Give the extent of all Plasmodium vivax-infected red blood cells.
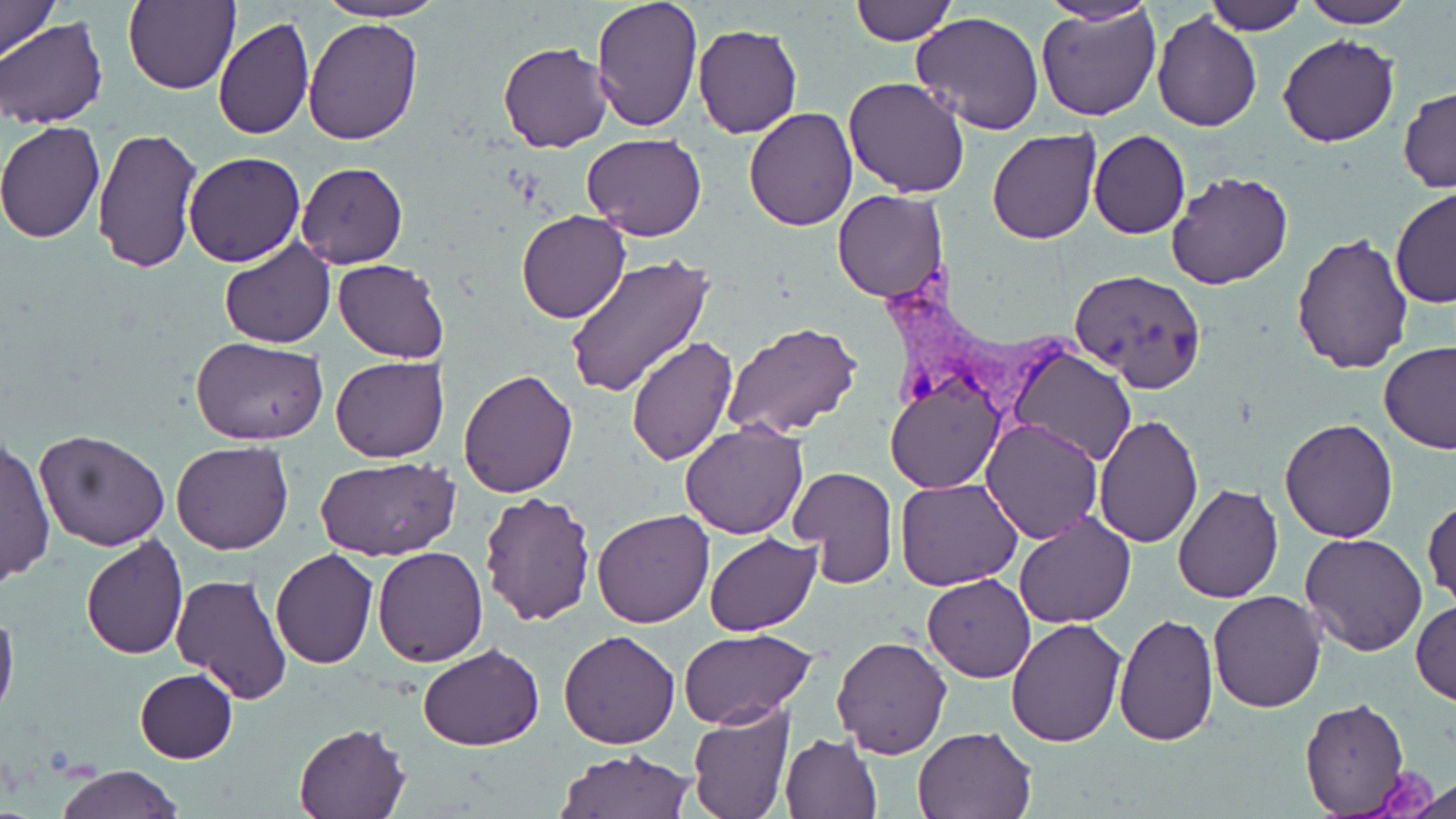
Approximate bounding boxes as named x1/y1/x2/y2 corners in pixels.
Plasmodium vivax-infected red blood cells: (x1=877, y1=263, x2=1085, y2=423).

Uninfected red blood cell locations: (x1=0, y1=0, x2=61, y2=61), (x1=316, y1=0, x2=446, y2=22), (x1=590, y1=0, x2=706, y2=135), (x1=1044, y1=0, x2=1154, y2=26), (x1=1204, y1=0, x2=1307, y2=35), (x1=1298, y1=0, x2=1414, y2=28), (x1=124, y1=1, x2=240, y2=92), (x1=849, y1=1, x2=957, y2=45), (x1=1037, y1=3, x2=1162, y2=121), (x1=1152, y1=11, x2=1262, y2=131), (x1=910, y1=12, x2=1045, y2=134), (x1=212, y1=17, x2=314, y2=138), (x1=1, y1=18, x2=107, y2=129), (x1=304, y1=18, x2=423, y2=144), (x1=693, y1=24, x2=802, y2=138), (x1=1278, y1=34, x2=1398, y2=148), (x1=497, y1=40, x2=612, y2=153), (x1=842, y1=77, x2=971, y2=198), (x1=1398, y1=86, x2=1456, y2=194), (x1=744, y1=105, x2=857, y2=231), (x1=0, y1=122, x2=105, y2=243), (x1=91, y1=127, x2=202, y2=275), (x1=986, y1=129, x2=1101, y2=244), (x1=1088, y1=131, x2=1191, y2=240), (x1=582, y1=133, x2=706, y2=240), (x1=184, y1=150, x2=306, y2=268), (x1=296, y1=163, x2=408, y2=268), (x1=1166, y1=173, x2=1293, y2=291), (x1=1389, y1=186, x2=1456, y2=310), (x1=832, y1=190, x2=949, y2=302), (x1=516, y1=210, x2=631, y2=325), (x1=1292, y1=235, x2=1414, y2=374), (x1=218, y1=237, x2=337, y2=348), (x1=565, y1=255, x2=713, y2=398), (x1=334, y1=259, x2=448, y2=363), (x1=1069, y1=271, x2=1208, y2=393), (x1=723, y1=321, x2=862, y2=439), (x1=188, y1=335, x2=330, y2=445), (x1=627, y1=337, x2=736, y2=466), (x1=1377, y1=341, x2=1456, y2=453), (x1=1009, y1=346, x2=1137, y2=468), (x1=330, y1=355, x2=449, y2=463), (x1=458, y1=370, x2=579, y2=497), (x1=885, y1=375, x2=1004, y2=494), (x1=1093, y1=414, x2=1202, y2=549), (x1=1280, y1=416, x2=1399, y2=542), (x1=980, y1=419, x2=1103, y2=543), (x1=679, y1=422, x2=809, y2=539), (x1=35, y1=429, x2=171, y2=550), (x1=1, y1=436, x2=54, y2=589), (x1=171, y1=440, x2=294, y2=554), (x1=316, y1=457, x2=459, y2=562), (x1=789, y1=465, x2=898, y2=588), (x1=896, y1=476, x2=1023, y2=591), (x1=1173, y1=483, x2=1284, y2=603), (x1=479, y1=491, x2=598, y2=628), (x1=1423, y1=496, x2=1456, y2=607), (x1=590, y1=510, x2=713, y2=628), (x1=1013, y1=510, x2=1136, y2=629), (x1=1300, y1=532, x2=1427, y2=655), (x1=703, y1=533, x2=820, y2=637), (x1=79, y1=536, x2=189, y2=659), (x1=373, y1=545, x2=489, y2=666), (x1=272, y1=548, x2=377, y2=668), (x1=169, y1=573, x2=290, y2=705), (x1=921, y1=574, x2=1035, y2=683), (x1=1207, y1=591, x2=1327, y2=712), (x1=1411, y1=600, x2=1456, y2=704), (x1=0, y1=604, x2=18, y2=719), (x1=1112, y1=612, x2=1219, y2=746), (x1=1005, y1=617, x2=1127, y2=748), (x1=679, y1=628, x2=816, y2=730), (x1=558, y1=629, x2=681, y2=748), (x1=830, y1=636, x2=954, y2=757), (x1=419, y1=643, x2=546, y2=749), (x1=134, y1=667, x2=237, y2=762), (x1=1299, y1=696, x2=1409, y2=817), (x1=686, y1=702, x2=796, y2=819), (x1=294, y1=721, x2=409, y2=818), (x1=912, y1=725, x2=1037, y2=817), (x1=779, y1=732, x2=883, y2=819), (x1=554, y1=748, x2=694, y2=818), (x1=55, y1=763, x2=181, y2=819), (x1=1387, y1=768, x2=1455, y2=818). Slide-level diagnosis: Plasmodium vivax. Thin blood film. 1000x magnification. Optical microscopy. One field of a larger specimen. May-Grünwald-Giemsa stain. Image is 1456×819 pixels.